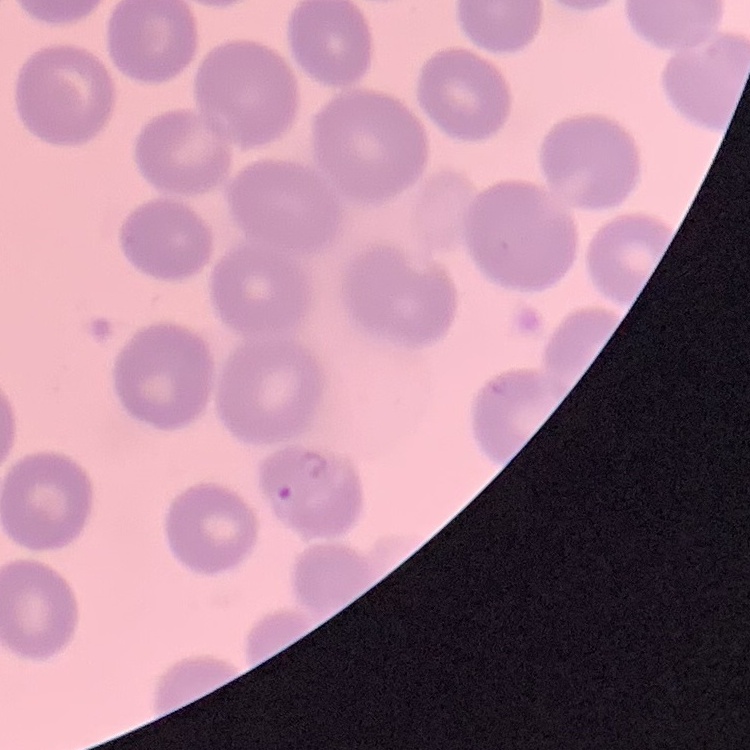

The red blood cells exhibit no rouleaux formation. Thin blood smear. Square crop of a larger photomicrograph. Field's or Giemsa stain.